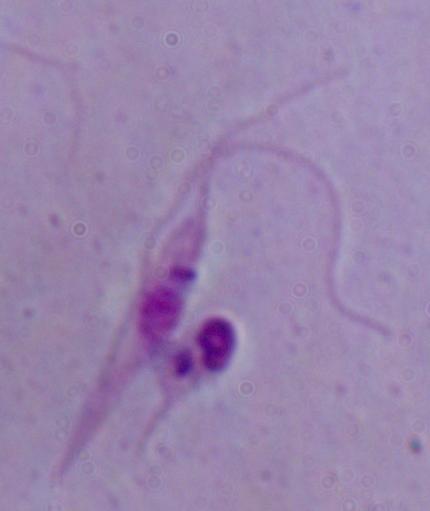
{
  "modality": "photomicrograph",
  "magnification": "1000x",
  "identification": "Leishmania"
}